Classify this cell by malaria status.
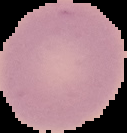

It is uninfected.

preparation = thin blood film
image size = 127×133 pixels
image type = cell region segmented out of the field of view; surrounding area masked to black